Give the extent of all Trypanosoma brucei.
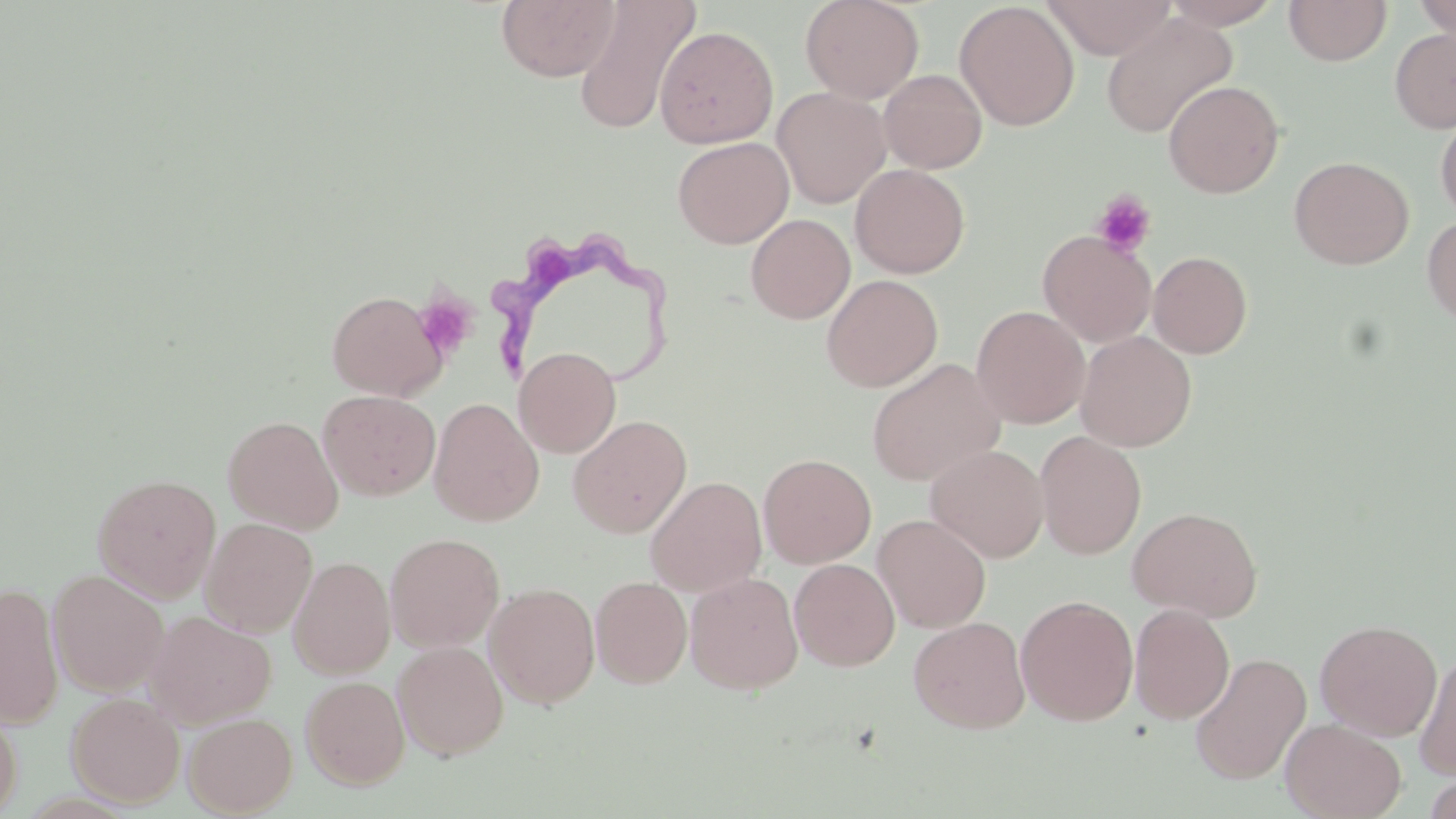
Approximate bounding boxes as named x1/y1/x2/y2 corners in pixels.
Trypanosoma brucei: (x1=492, y1=234, x2=674, y2=393).

{
  "slide_level_diagnosis": "Trypanosoma brucei",
  "modality": "optical microscopy",
  "field_of_view": "one of a larger specimen",
  "stain": "May-Grünwald-Giemsa",
  "preparation": "thin blood film",
  "uninfected_red_blood_cell_locations": "approximate bounding boxes as named x1/y1/x2/y2 corners in pixels: (x1=497, y1=0, x2=620, y2=82), (x1=572, y1=0, x2=699, y2=135), (x1=800, y1=0, x2=924, y2=104), (x1=1041, y1=0, x2=1176, y2=60), (x1=1161, y1=0, x2=1284, y2=29), (x1=955, y1=1, x2=1079, y2=131), (x1=1283, y1=1, x2=1392, y2=66), (x1=1411, y1=1, x2=1455, y2=42), (x1=1101, y1=13, x2=1237, y2=139), (x1=655, y1=25, x2=778, y2=148), (x1=1390, y1=27, x2=1456, y2=133), (x1=879, y1=69, x2=987, y2=173), (x1=1164, y1=80, x2=1284, y2=198), (x1=771, y1=86, x2=891, y2=208), (x1=1435, y1=112, x2=1456, y2=222), (x1=673, y1=136, x2=794, y2=249), (x1=1289, y1=156, x2=1413, y2=269), (x1=850, y1=163, x2=970, y2=278), (x1=746, y1=214, x2=855, y2=324), (x1=1422, y1=214, x2=1456, y2=327), (x1=1038, y1=230, x2=1156, y2=346), (x1=1148, y1=251, x2=1253, y2=358), (x1=821, y1=274, x2=942, y2=392), (x1=327, y1=290, x2=447, y2=401), (x1=971, y1=305, x2=1090, y2=428), (x1=1076, y1=330, x2=1197, y2=452), (x1=514, y1=346, x2=621, y2=458), (x1=867, y1=358, x2=1006, y2=486), (x1=318, y1=389, x2=441, y2=501), (x1=428, y1=397, x2=544, y2=526), (x1=223, y1=415, x2=344, y2=534), (x1=568, y1=415, x2=692, y2=538), (x1=1035, y1=431, x2=1147, y2=559), (x1=925, y1=444, x2=1049, y2=563), (x1=758, y1=453, x2=876, y2=569), (x1=92, y1=473, x2=221, y2=602), (x1=645, y1=476, x2=767, y2=596), (x1=1128, y1=506, x2=1264, y2=622), (x1=873, y1=513, x2=991, y2=633), (x1=200, y1=517, x2=318, y2=636), (x1=385, y1=533, x2=504, y2=652), (x1=287, y1=550, x2=503, y2=663), (x1=288, y1=556, x2=395, y2=679), (x1=789, y1=558, x2=900, y2=670), (x1=48, y1=569, x2=169, y2=697), (x1=685, y1=571, x2=804, y2=694), (x1=590, y1=576, x2=692, y2=688), (x1=0, y1=582, x2=64, y2=728), (x1=484, y1=582, x2=601, y2=709), (x1=1015, y1=595, x2=1139, y2=726), (x1=1129, y1=604, x2=1236, y2=725), (x1=145, y1=610, x2=276, y2=727), (x1=908, y1=616, x2=1031, y2=733), (x1=1315, y1=619, x2=1442, y2=740), (x1=392, y1=641, x2=508, y2=760), (x1=1413, y1=650, x2=1456, y2=781), (x1=1189, y1=652, x2=1311, y2=785), (x1=300, y1=675, x2=410, y2=789), (x1=66, y1=692, x2=185, y2=808), (x1=0, y1=706, x2=22, y2=818), (x1=183, y1=711, x2=297, y2=817), (x1=1280, y1=718, x2=1406, y2=819), (x1=1423, y1=773, x2=1456, y2=819)",
  "magnification": "1000x",
  "image_size": "1456×819 pixels",
  "platelet_locations": "approximate bounding boxes as named x1/y1/x2/y2 corners in pixels: (x1=1092, y1=190, x2=1156, y2=257), (x1=413, y1=294, x2=476, y2=358)"
}